Assess for malaria.
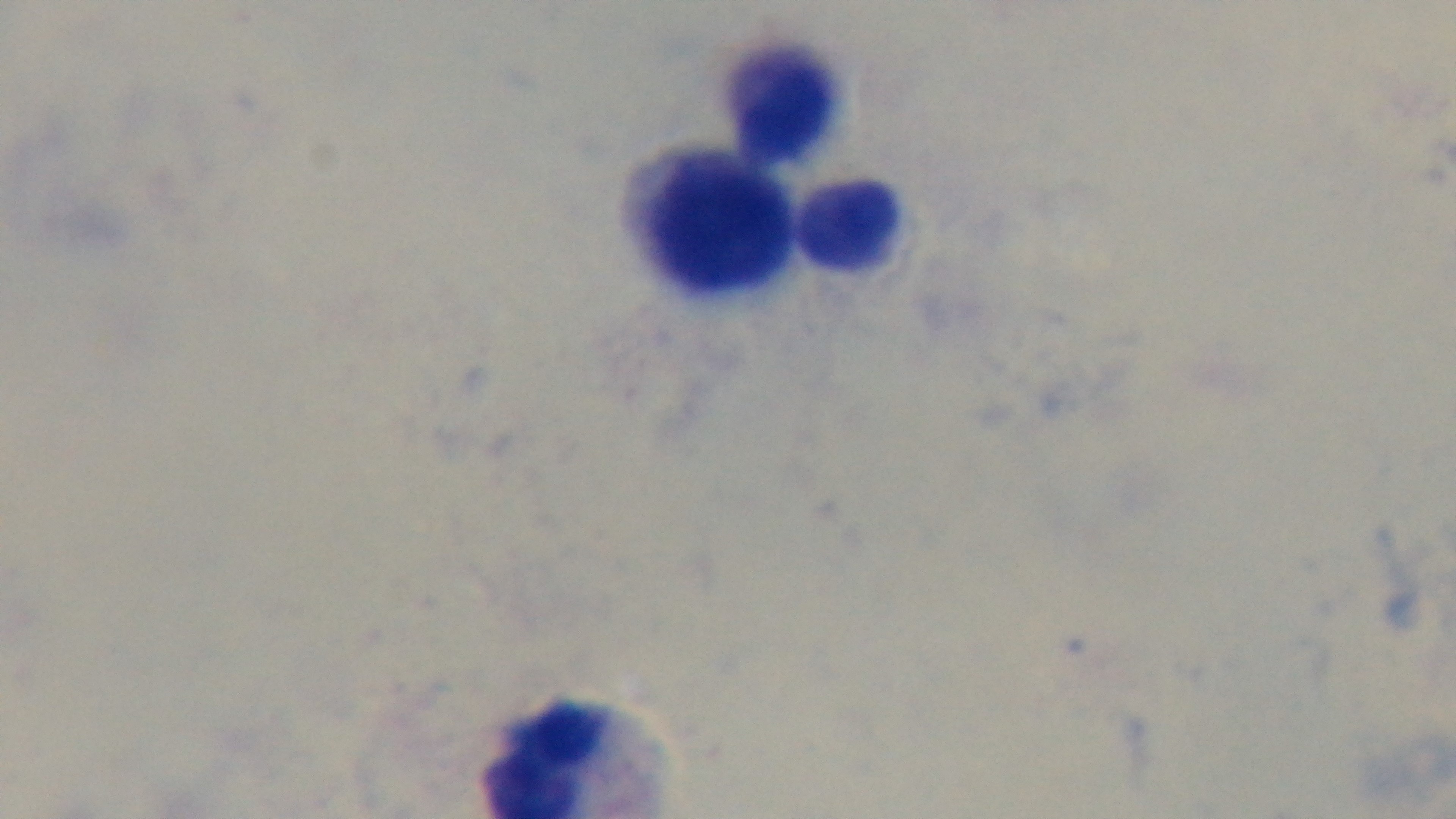

Uninfected.

Summary:
  - Preparation: thick smear
  - Modality: light microscopy
  - Field of view: one from the slide
  - Capture: mounted 4K digital camera
  - Objective: 100x oil immersion
  - Stain: Giemsa